Locate every leukocyte (white blood cell).
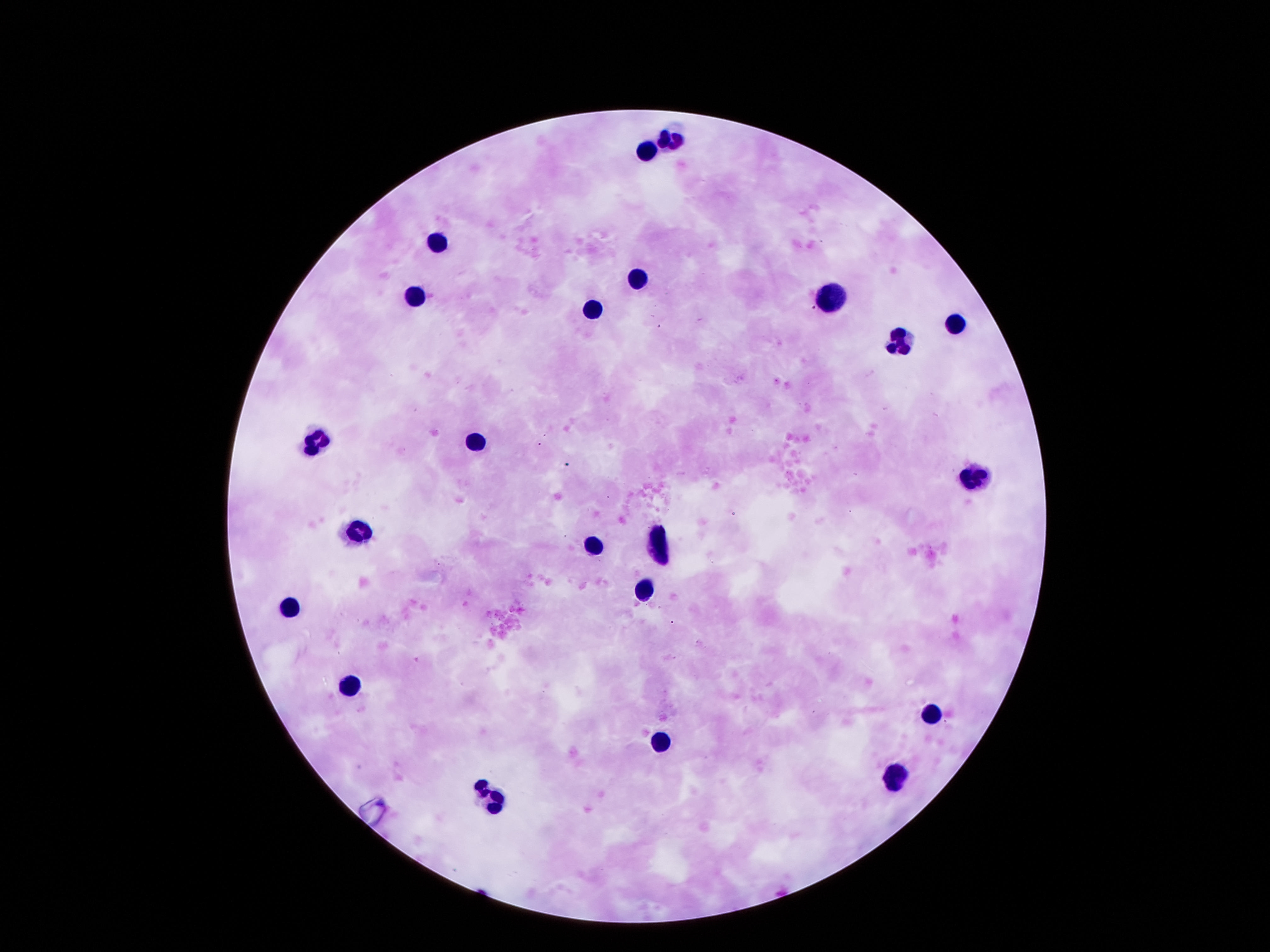

Approximate centers as (x, y) in pixels.
Leukocytes: (671, 137), (647, 149), (439, 239), (635, 275), (412, 295), (824, 296), (590, 304), (959, 325), (902, 343), (313, 436), (475, 440), (974, 473), (358, 530), (593, 544), (659, 548), (641, 586), (286, 605), (346, 682), (932, 710), (662, 734), (890, 778), (487, 796).

Thick blood smear. Single field of view. Giemsa stain. Patient malaria status: negative. 100x magnification. Smartphone photograph taken through the microscope eyepiece. Image is 1270×952 pixels.